State the preparation type.
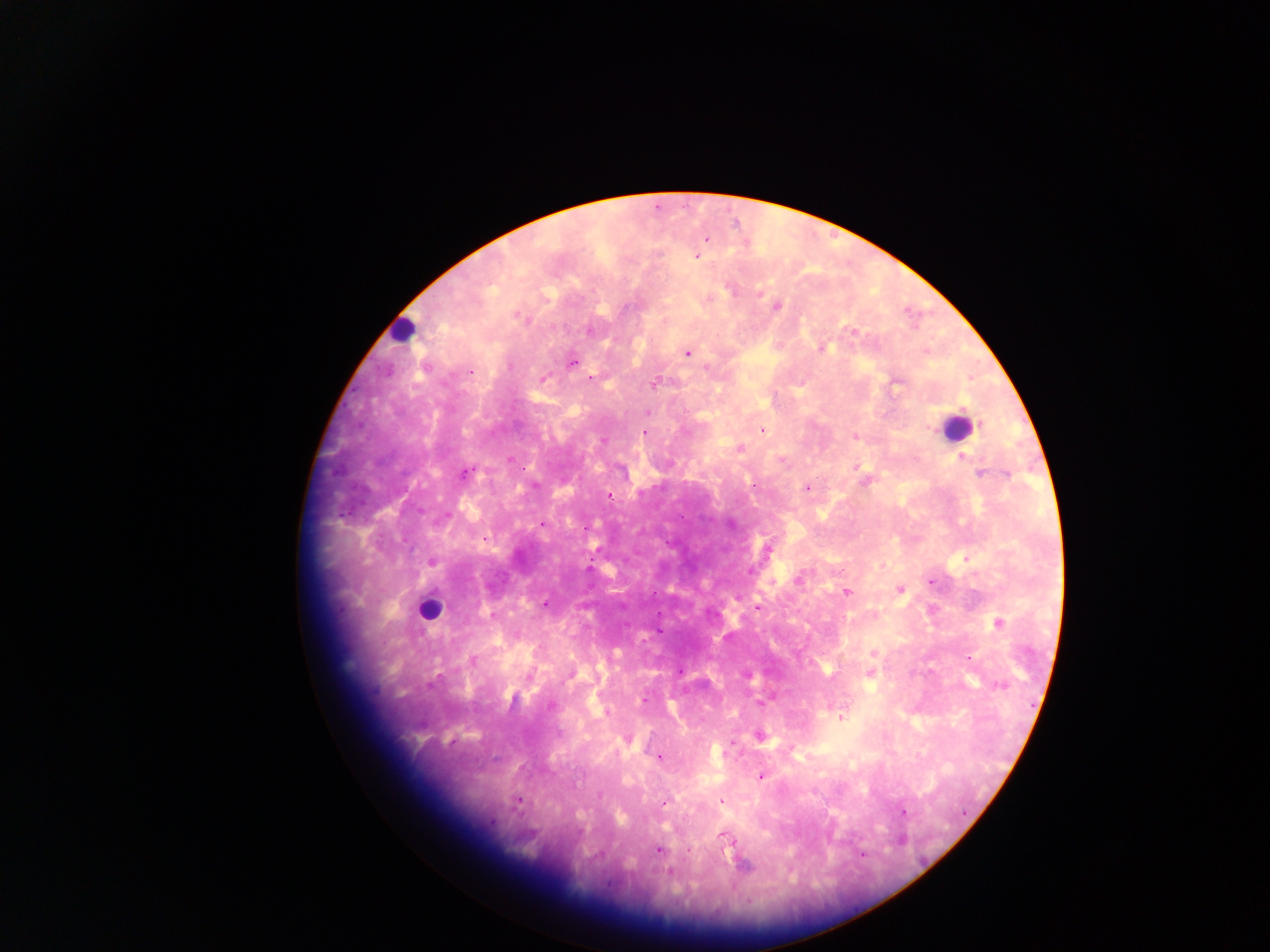
Thick blood smear.

Approximate centers as x y in pixels. Leukocyte locations: 402 329; 956 427; 428 609. Plasmodium parasite locations: 707 239; 697 257; 730 289; 760 293; 777 307; 590 331; 853 331; 822 348; 687 353; 572 363; 706 368; 470 372; 543 379; 591 379; 654 383; 896 384; 647 413; 763 431; 644 432; 855 437; 740 449; 961 457; 511 460; 781 461; 856 467; 465 473; 980 474; 1007 474; 535 485; 807 488; 609 495; 542 525; 585 527; 485 538; 767 550; 432 562; 751 571; 799 578; 931 581; 900 590; 846 592; 545 604; 758 609; 492 615; 997 623; 874 653; 970 658; 473 659; 680 672; 869 674; 570 675; 748 676; 1001 685; 644 699; 761 704; 551 705; 607 712; 842 716; 759 736; 659 757; 760 777; 599 795; 518 801; 664 802; 722 802; 904 812; 723 836; 658 850; 688 851; 861 854; 669 872. Image is 1270×952 pixels. Mobile-phone photograph taken through the microscope. Collected in Ghana. Single field of view.